Assess this cell for malaria.
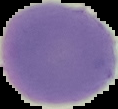

Uninfected.

image_size: 118×109 pixels
preparation: thin blood film
image_type: cell region segmented out of the field of view; surrounding area masked to black